Locate every blood parasite and identify its species.
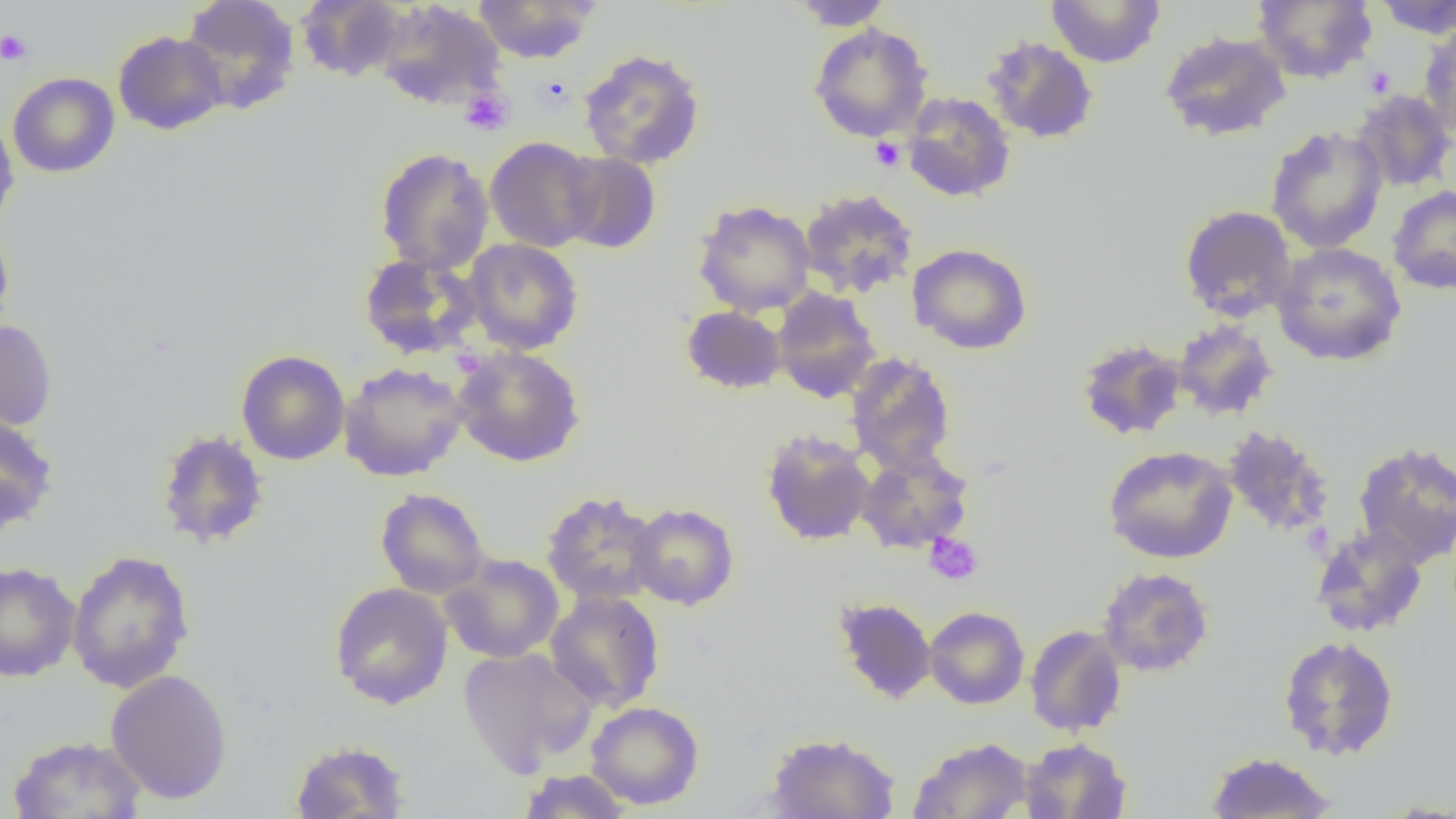
No blood parasites seen.

{
  "slide_level_diagnosis": "negative for blood parasites",
  "magnification": "1000x",
  "modality": "light microscopy",
  "preparation": "thin blood smear",
  "uninfected_red_blood_cell_locations": "approximate bounding boxes as (x1,y1)-(x2,y2) corner pairs in pixels: (180,0)-(301,113), (295,0)-(407,83), (472,0)-(600,63), (789,0)-(895,31), (1046,0)-(1165,67), (1251,0)-(1377,84), (1372,0)-(1456,39), (374,1)-(506,111), (809,23)-(932,142), (1419,23)-(1456,140), (113,30)-(228,135), (1159,30)-(1291,142), (982,36)-(1099,144), (578,49)-(706,170), (8,72)-(119,178), (1350,89)-(1455,193), (901,92)-(1015,202), (0,116)-(19,232), (1265,125)-(1388,254), (485,136)-(601,252), (375,147)-(494,274), (558,151)-(661,254), (1387,185)-(1456,296), (798,188)-(919,299), (693,199)-(816,317), (1179,204)-(1298,323), (0,223)-(15,338), (462,238)-(584,355), (1272,242)-(1407,366), (907,243)-(1033,355), (358,252)-(482,359), (771,288)-(882,403), (681,305)-(787,395), (0,320)-(58,432), (1172,320)-(1278,421), (1076,338)-(1186,441), (452,345)-(585,467), (236,350)-(350,465), (845,352)-(957,476), (339,361)-(469,482), (0,412)-(58,535), (1221,425)-(1335,538), (760,428)-(875,546), (155,429)-(269,550), (1352,440)-(1456,566), (1102,445)-(1238,564), (855,449)-(973,554), (375,488)-(489,599), (541,490)-(662,607), (627,502)-(739,610), (1310,523)-(1429,639), (66,549)-(195,694), (441,553)-(564,663), (0,561)-(82,683), (1097,566)-(1214,677), (329,582)-(453,710), (545,591)-(665,713), (832,596)-(937,704), (924,606)-(1029,709), (1024,625)-(1127,736), (1278,636)-(1399,760), (458,647)-(597,776), (105,669)-(233,805), (586,701)-(704,809), (764,731)-(901,818), (7,734)-(147,819), (908,737)-(1033,819), (1019,737)-(1131,818), (290,739)-(410,818), (1205,751)-(1336,818), (516,768)-(633,818), (1372,798)-(1456,817)",
  "field_of_view": "single",
  "image_size": "1456×819 pixels",
  "platelet_locations": "approximate bounding boxes as (x1,y1)-(x2,y2) corner pairs in pixels: (0,29)-(34,66), (1363,65)-(1395,97), (459,88)-(514,135), (870,137)-(905,172), (924,532)-(983,585)"
}